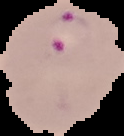
Image is 124×136 pixels. From a thin blood smear. Result: malaria parasites detected. Cell region segmented out of the field of view; the surrounding area is masked to black.